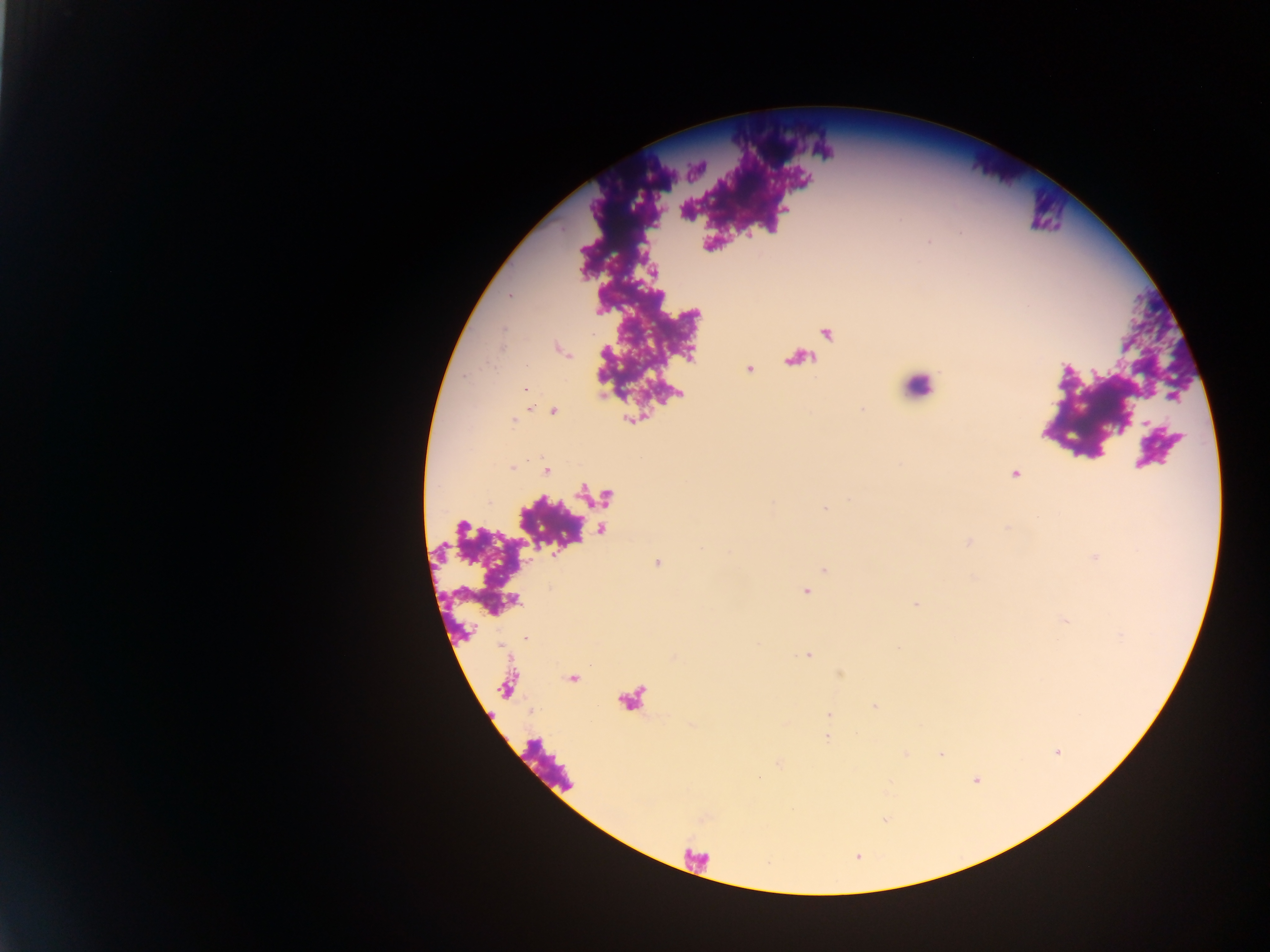

Approximate centers as (x, y) in pixels.
Summary:
  - Leukocyte locations: (918, 386)
  - Plasmodium parasite locations: (929, 241), (509, 296), (524, 390), (553, 412), (514, 421), (511, 468), (546, 470), (1015, 474), (825, 508), (806, 592), (915, 605), (526, 637), (809, 656), (828, 715), (826, 737)
  - Image size: 1270×952 pixels
  - Country: Ghana
  - Field of view: single
  - Preparation: thick blood film
  - Capture: mobile-phone photograph through a microscope